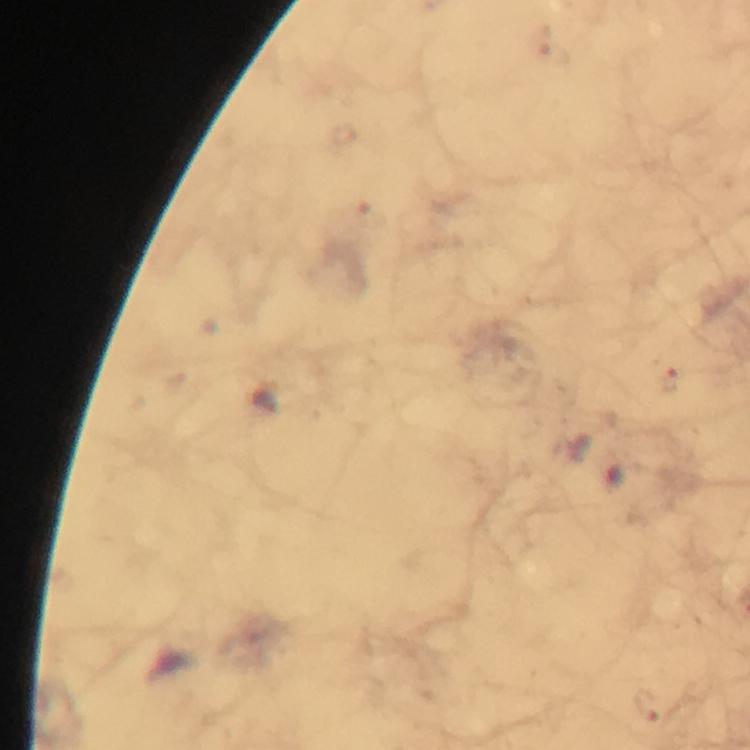
Approximate centers as {x, y} in pixels. Malaria parasite locations: {668, 380}, {648, 704}. Giemsa-stained preparation. Thick smear. A crop from one field of view. Photographed through the microscope with a smartphone camera. At 100x magnification. Immersion oil was used. From a diagnostic examination for malaria. Image is 750×750 pixels.